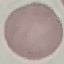

Summary:
  - Result: no malaria parasites seen
  - Image type: automatically extracted cell patch, resized to 64 × 64 pixels
  - Preparation: thin smear
  - Stain: Giemsa
  - Capture: smartphone camera at the microscope eyepiece